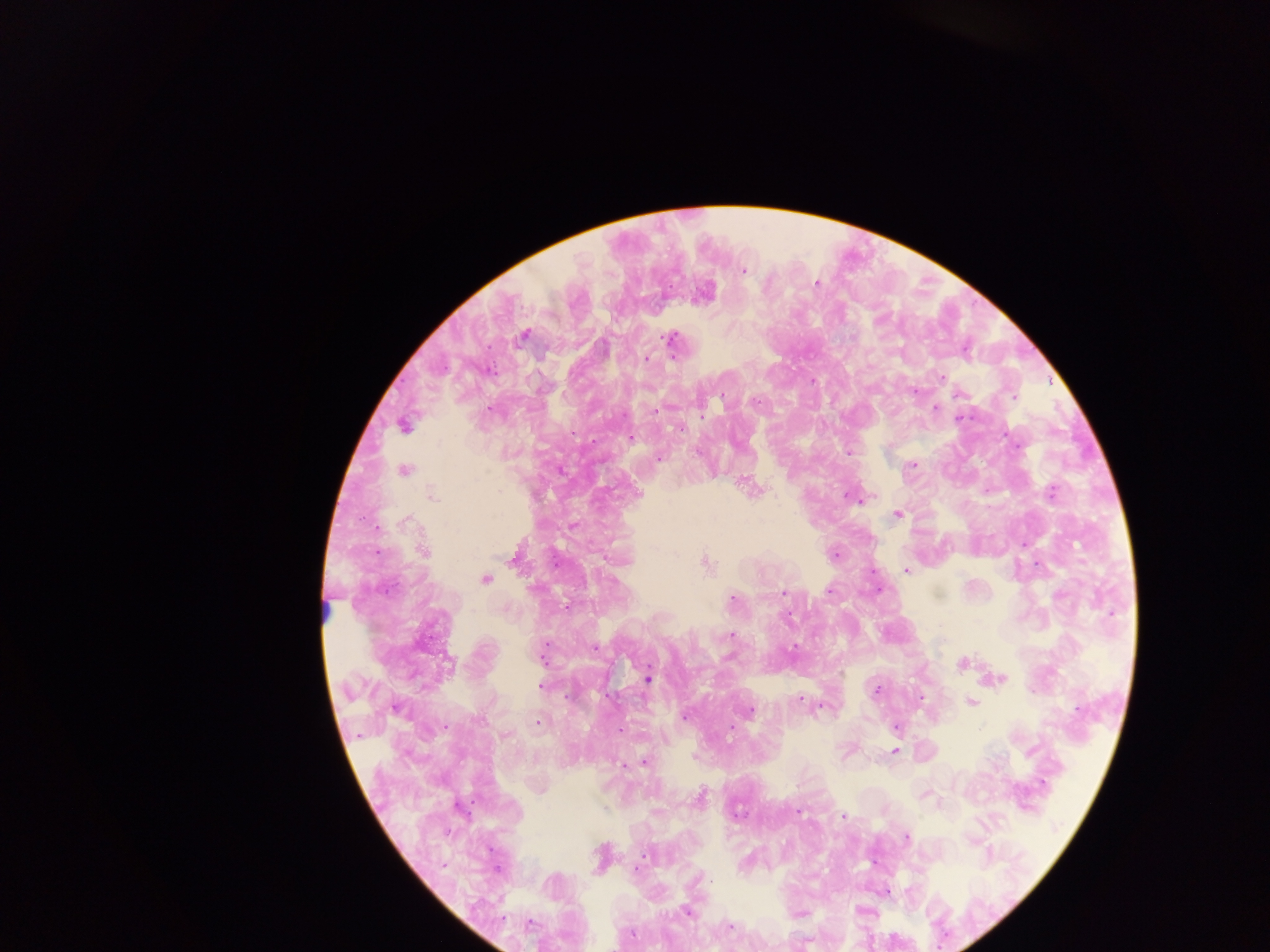
{
  "capture": "mobile-phone photograph through a microscope",
  "country": "Ghana",
  "plasmodium_parasite_locations": "approximate centers as {x, y} in pixels: {743, 270}, {816, 283}, {704, 293}, {524, 336}, {670, 339}, {646, 359}, {940, 378}, {914, 391}, {722, 394}, {958, 394}, {1013, 396}, {935, 408}, {655, 411}, {961, 417}, {403, 425}, {680, 428}, {630, 438}, {847, 453}, {659, 458}, {910, 465}, {403, 470}, {751, 487}, {1051, 492}, {431, 495}, {857, 499}, {898, 513}, {406, 521}, {572, 526}, {422, 551}, {834, 554}, {515, 557}, {705, 563}, {907, 569}, {485, 578}, {829, 590}, {878, 590}, {783, 592}, {731, 598}, {788, 616}, {731, 634}, {794, 647}, {593, 648}, {542, 652}, {962, 662}, {646, 678}, {994, 679}, {540, 686}, {877, 691}, {800, 698}, {920, 698}, {972, 703}, {747, 711}, {684, 715}, {538, 722}, {732, 726}, {895, 726}, {620, 731}, {894, 751}, {645, 762}, {622, 763}, {924, 793}, {699, 798}, {797, 812}, {844, 816}, {906, 836}, {600, 856}, {637, 868}, {885, 892}, {687, 912}, {798, 913}, {729, 927}",
  "field_of_view": "single",
  "image_size": "1270×952 pixels",
  "preparation": "thick blood smear"
}